Classify this cell by malaria status.
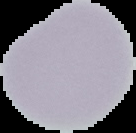
Uninfected.

image type = cell region segmented out of the field of view; surrounding area masked to black
image size = 136×133 pixels
preparation = thin blood smear